Classify this cell by malaria status.
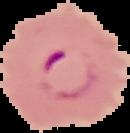
It is parasitized.

image_type: cell region segmented out of the field of view; surrounding area masked to black
image_size: 130×133 pixels
preparation: thin blood smear